Identify the preparation type.
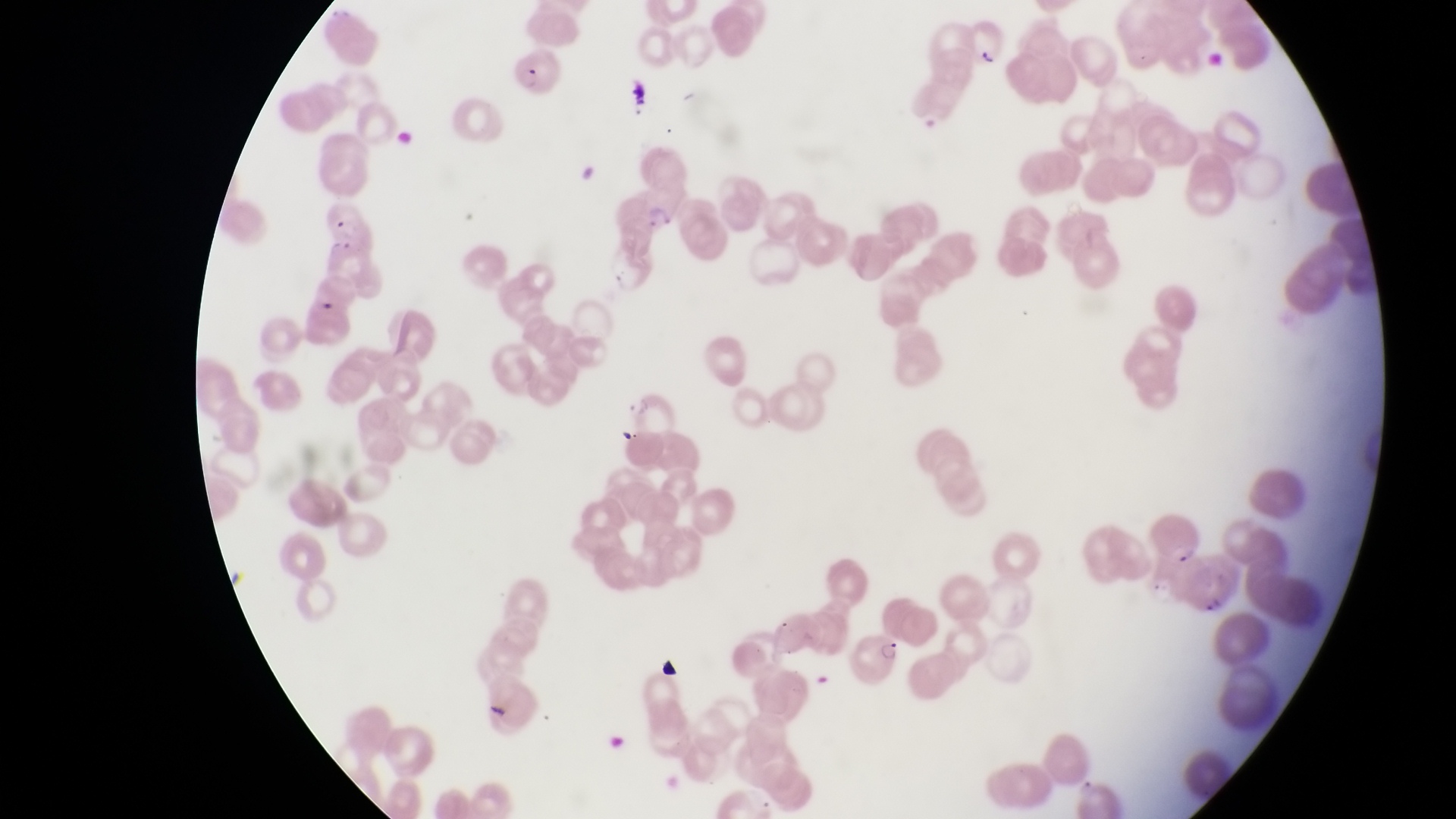

This is a thin smear.

{
  "trophozoite_locations": "approximate bounding boxes as left top right bottom in pixels: 629 100 653 123",
  "artifact_platelet_like_body_stain_precipitate_or_debris_locations": "approximate bounding boxes as left top right bottom in pixels: 570 159 597 185; 486 701 519 727",
  "image_size": "1456×819 pixels",
  "parasitised_red_blood_cell_locations": "approximate bounding boxes as left top right bottom in pixels: 512 45 558 98; 634 185 679 232; 320 199 372 249; 621 386 676 435; 1149 507 1205 571; 851 629 906 685",
  "field_of_view": "single",
  "magnification": "1000x",
  "country": "Uganda",
  "capture": "smartphone photograph through the eyepiece of an Olympus CX-23 microscope"
}